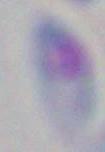
Summary:
  - Identification: Toxoplasma gondii
  - Modality: micrograph
  - Magnification: 1000x